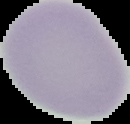

Malaria status: uninfected. Segmented cell region on a black background. From a thin blood smear. Image is 130×124 pixels.